Identify the parasite.
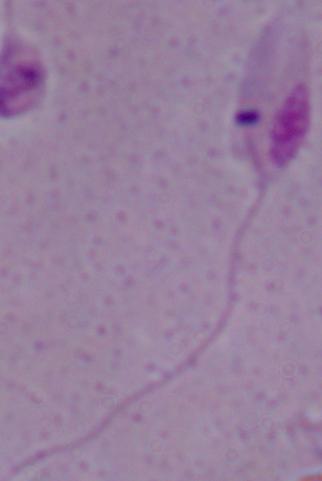

Leishmania.

magnification: 1000x
modality: micrograph